Classify this cell by malaria status.
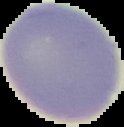

It is uninfected.

preparation: thin blood smear
image_size: 124×127 pixels
image_type: cell region segmented out of the field of view; surrounding area masked to black